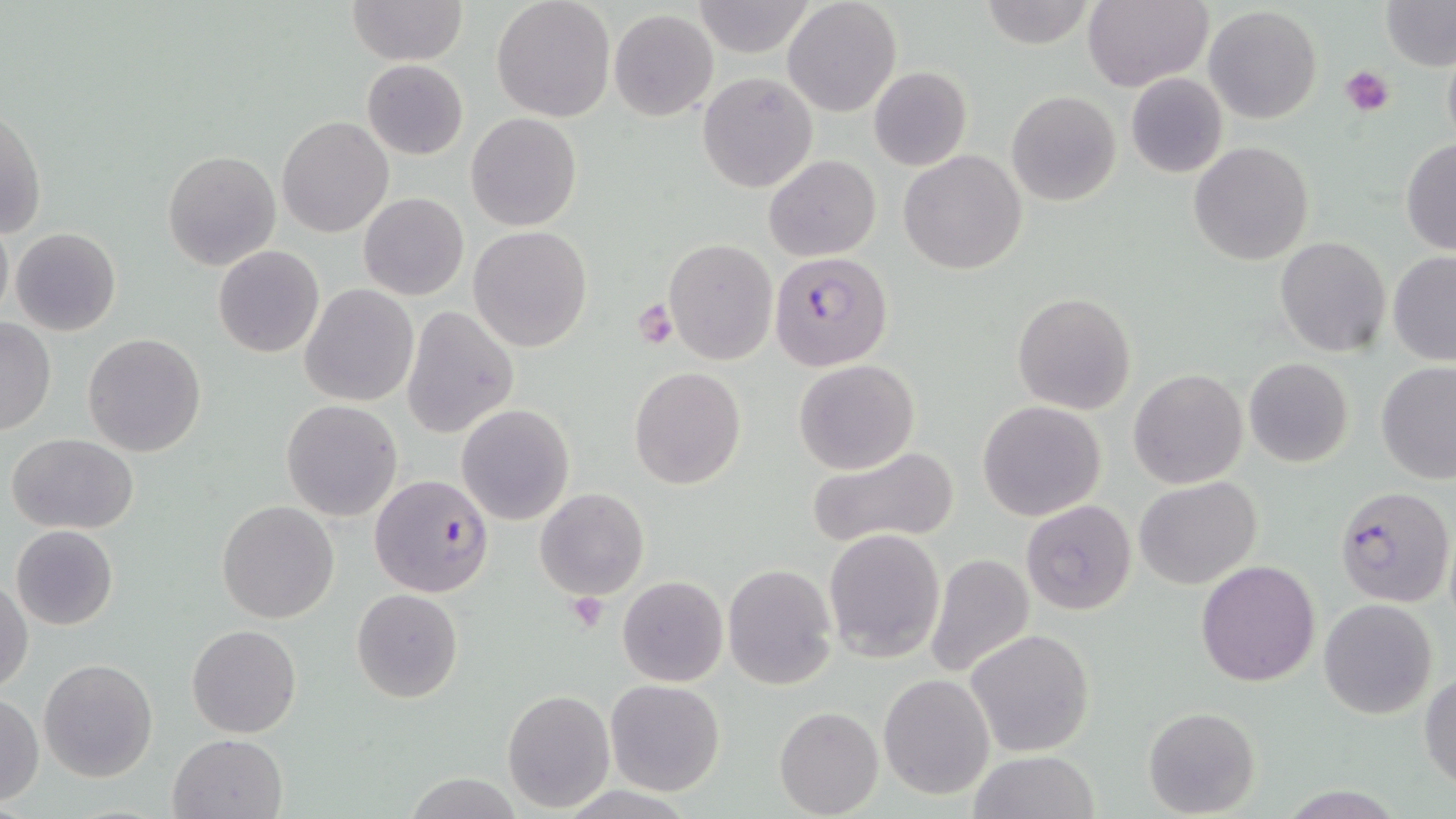 Approximate bounding boxes as named x1/y1/x2/y2 corners in pixels. Uninfected red blood cell locations: (x1=349, y1=0, x2=467, y2=67), (x1=492, y1=0, x2=615, y2=121), (x1=782, y1=0, x2=901, y2=118), (x1=981, y1=0, x2=1097, y2=49), (x1=1082, y1=0, x2=1212, y2=91), (x1=1379, y1=0, x2=1455, y2=71), (x1=690, y1=1, x2=815, y2=57), (x1=1204, y1=6, x2=1323, y2=126), (x1=608, y1=10, x2=720, y2=121), (x1=1442, y1=40, x2=1456, y2=159), (x1=362, y1=59, x2=468, y2=159), (x1=868, y1=66, x2=973, y2=172), (x1=698, y1=71, x2=818, y2=193), (x1=1126, y1=73, x2=1228, y2=177), (x1=1006, y1=90, x2=1121, y2=206), (x1=1, y1=108, x2=45, y2=240), (x1=465, y1=112, x2=582, y2=231), (x1=277, y1=116, x2=394, y2=238), (x1=1400, y1=140, x2=1456, y2=254), (x1=1189, y1=141, x2=1313, y2=266), (x1=162, y1=149, x2=280, y2=271), (x1=899, y1=149, x2=1026, y2=276), (x1=764, y1=155, x2=881, y2=260), (x1=358, y1=192, x2=468, y2=301), (x1=0, y1=213, x2=12, y2=324), (x1=469, y1=226, x2=594, y2=352), (x1=10, y1=227, x2=121, y2=336), (x1=1274, y1=236, x2=1391, y2=357), (x1=663, y1=238, x2=779, y2=366), (x1=213, y1=245, x2=324, y2=358), (x1=1387, y1=252, x2=1456, y2=366), (x1=300, y1=284, x2=418, y2=405), (x1=1013, y1=292, x2=1136, y2=415), (x1=402, y1=305, x2=519, y2=438), (x1=0, y1=318, x2=56, y2=438), (x1=83, y1=332, x2=207, y2=457), (x1=794, y1=358, x2=919, y2=474), (x1=1244, y1=358, x2=1353, y2=468), (x1=1376, y1=361, x2=1456, y2=484), (x1=628, y1=366, x2=745, y2=490), (x1=1128, y1=368, x2=1248, y2=489), (x1=281, y1=400, x2=402, y2=520), (x1=977, y1=400, x2=1107, y2=522), (x1=456, y1=404, x2=575, y2=527), (x1=5, y1=433, x2=139, y2=534), (x1=804, y1=444, x2=963, y2=550), (x1=1134, y1=477, x2=1261, y2=590), (x1=535, y1=487, x2=649, y2=600), (x1=216, y1=499, x2=340, y2=623), (x1=1021, y1=499, x2=1137, y2=615), (x1=11, y1=525, x2=119, y2=630), (x1=823, y1=527, x2=945, y2=663), (x1=925, y1=552, x2=1034, y2=680), (x1=1196, y1=559, x2=1322, y2=687), (x1=722, y1=564, x2=837, y2=689), (x1=618, y1=576, x2=728, y2=687), (x1=1, y1=580, x2=33, y2=695), (x1=351, y1=588, x2=463, y2=704), (x1=1318, y1=598, x2=1438, y2=718), (x1=187, y1=623, x2=301, y2=738), (x1=966, y1=628, x2=1094, y2=756), (x1=39, y1=658, x2=159, y2=783), (x1=1419, y1=671, x2=1456, y2=790), (x1=879, y1=673, x2=996, y2=799), (x1=605, y1=679, x2=726, y2=797), (x1=502, y1=689, x2=615, y2=811), (x1=1, y1=693, x2=43, y2=804), (x1=774, y1=705, x2=883, y2=818), (x1=1143, y1=707, x2=1260, y2=817), (x1=168, y1=732, x2=290, y2=819), (x1=971, y1=750, x2=1098, y2=819), (x1=407, y1=774, x2=521, y2=817). Platelet locations: (x1=1340, y1=65, x2=1394, y2=117), (x1=632, y1=297, x2=680, y2=349), (x1=568, y1=591, x2=608, y2=631). Plasmodium falciparum-infected red blood cell locations: (x1=768, y1=251, x2=893, y2=372), (x1=368, y1=472, x2=495, y2=598), (x1=1333, y1=485, x2=1454, y2=607). Slide-level diagnosis: Plasmodium falciparum. Single field of view. Captured at 1000x magnification. Image is 1456×819 pixels. May-Grünwald-Giemsa stain. Light microscopy. Thin blood smear.